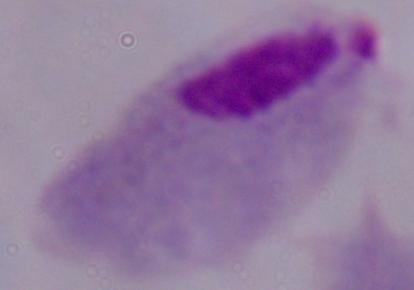

Summary:
  - Magnification: 1000x
  - Modality: micrograph
  - Identification: trichomonad